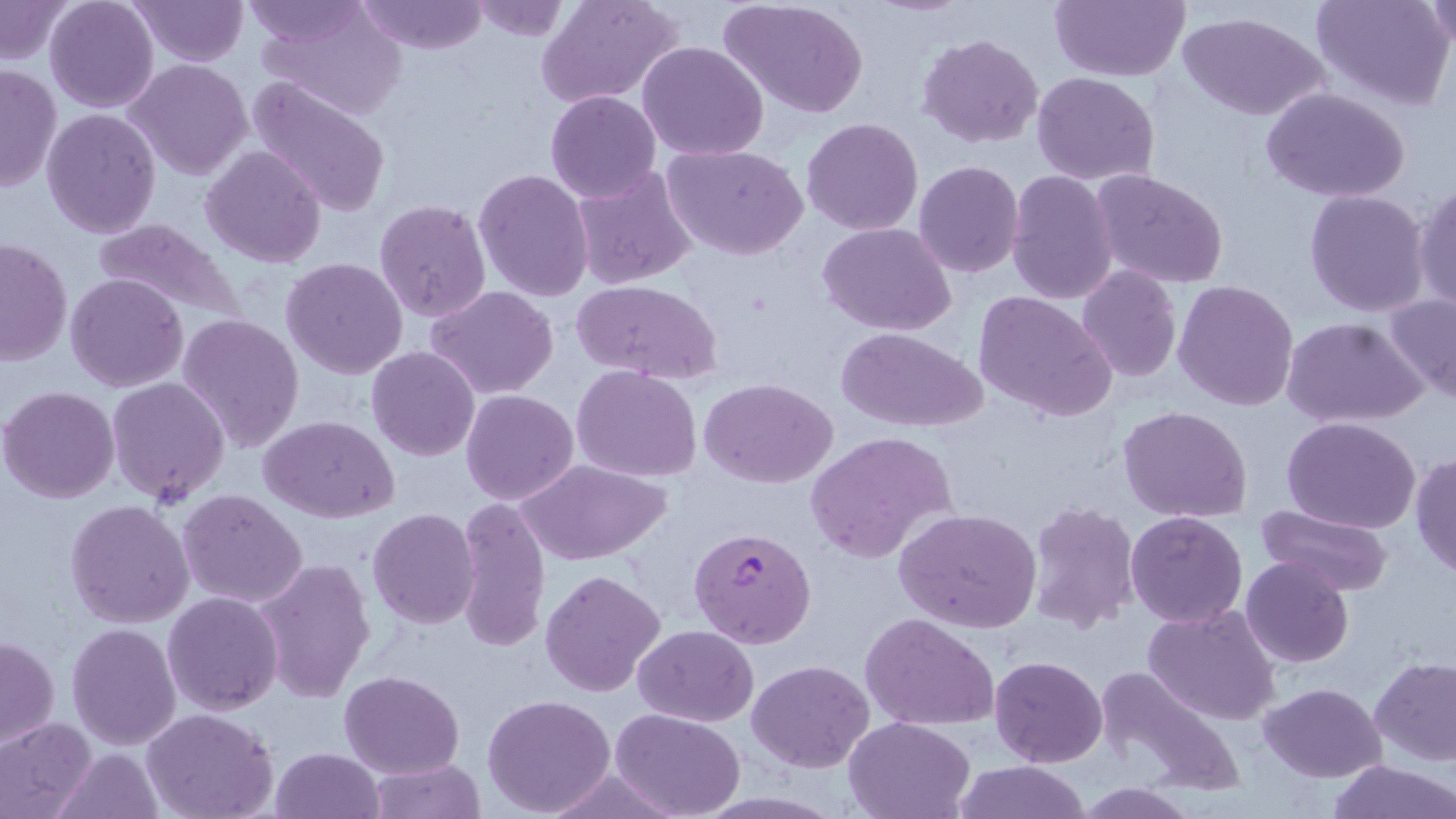

slide-level diagnosis = Plasmodium falciparum
uninfected red blood cell locations = approximate bounding boxes as (x1, y1, x2, y2) in pixels: (46, 0, 159, 113), (128, 0, 248, 67), (238, 0, 365, 44), (252, 0, 410, 120), (361, 0, 489, 55), (720, 0, 870, 118), (1049, 0, 1191, 82), (1311, 0, 1455, 112), (1423, 0, 1453, 51), (0, 1, 75, 64), (537, 1, 683, 108), (468, 2, 573, 44), (1179, 11, 1329, 122), (917, 33, 1044, 150), (637, 41, 769, 163), (124, 59, 254, 182), (0, 63, 61, 194), (1032, 72, 1161, 187), (245, 74, 392, 217), (1262, 87, 1410, 204), (545, 90, 663, 204), (42, 107, 162, 238), (802, 117, 924, 236), (661, 143, 808, 260), (200, 145, 327, 267), (914, 160, 1025, 278), (570, 164, 697, 289), (473, 168, 594, 304), (1090, 169, 1229, 291), (1006, 171, 1118, 304), (1412, 178, 1456, 313), (1305, 188, 1432, 317), (374, 199, 491, 322), (92, 219, 244, 327), (817, 222, 957, 334), (1, 238, 71, 366), (281, 257, 408, 380), (1077, 265, 1181, 383), (65, 273, 189, 392), (571, 279, 721, 384), (1172, 279, 1299, 411), (425, 284, 560, 399), (1382, 292, 1456, 405), (972, 293, 1117, 423), (177, 313, 306, 454), (1282, 316, 1429, 427), (837, 327, 986, 432), (366, 346, 481, 462), (573, 366, 702, 481), (108, 377, 229, 507), (701, 378, 838, 489), (0, 385, 120, 503), (461, 390, 579, 506), (1119, 405, 1254, 524), (259, 416, 399, 524), (1282, 417, 1423, 535), (804, 430, 959, 562), (1410, 450, 1456, 580), (522, 459, 669, 566), (178, 489, 307, 609), (454, 496, 553, 652), (66, 498, 196, 629), (1026, 501, 1141, 633), (1252, 503, 1395, 598), (894, 507, 1043, 633), (367, 508, 480, 629), (1125, 511, 1248, 628), (1240, 557, 1354, 669), (253, 558, 375, 704), (541, 569, 667, 697), (162, 591, 283, 716), (1142, 603, 1282, 725), (863, 613, 1000, 730), (66, 624, 181, 749), (633, 625, 759, 727), (1, 634, 60, 751), (991, 656, 1107, 766), (1370, 656, 1456, 765), (747, 659, 874, 772), (1092, 665, 1249, 801), (341, 668, 463, 779), (1258, 682, 1387, 781), (482, 693, 615, 816), (610, 708, 746, 818), (142, 709, 278, 819), (844, 716, 975, 819), (0, 717, 97, 818), (269, 747, 384, 819), (52, 748, 164, 819), (366, 759, 487, 817), (1328, 759, 1456, 818), (951, 761, 1093, 819), (1075, 783, 1199, 818)
modality = light microscopy
stain = May-Grünwald-Giemsa
Plasmodium falciparum-infected red blood cell locations = approximate bounding boxes as (x1, y1, x2, y2) in pixels: (689, 526, 815, 649)
preparation = thin blood film
magnification = 1000x
image size = 1456×819 pixels
field of view = single